Locate every blood parasite and identify its species.
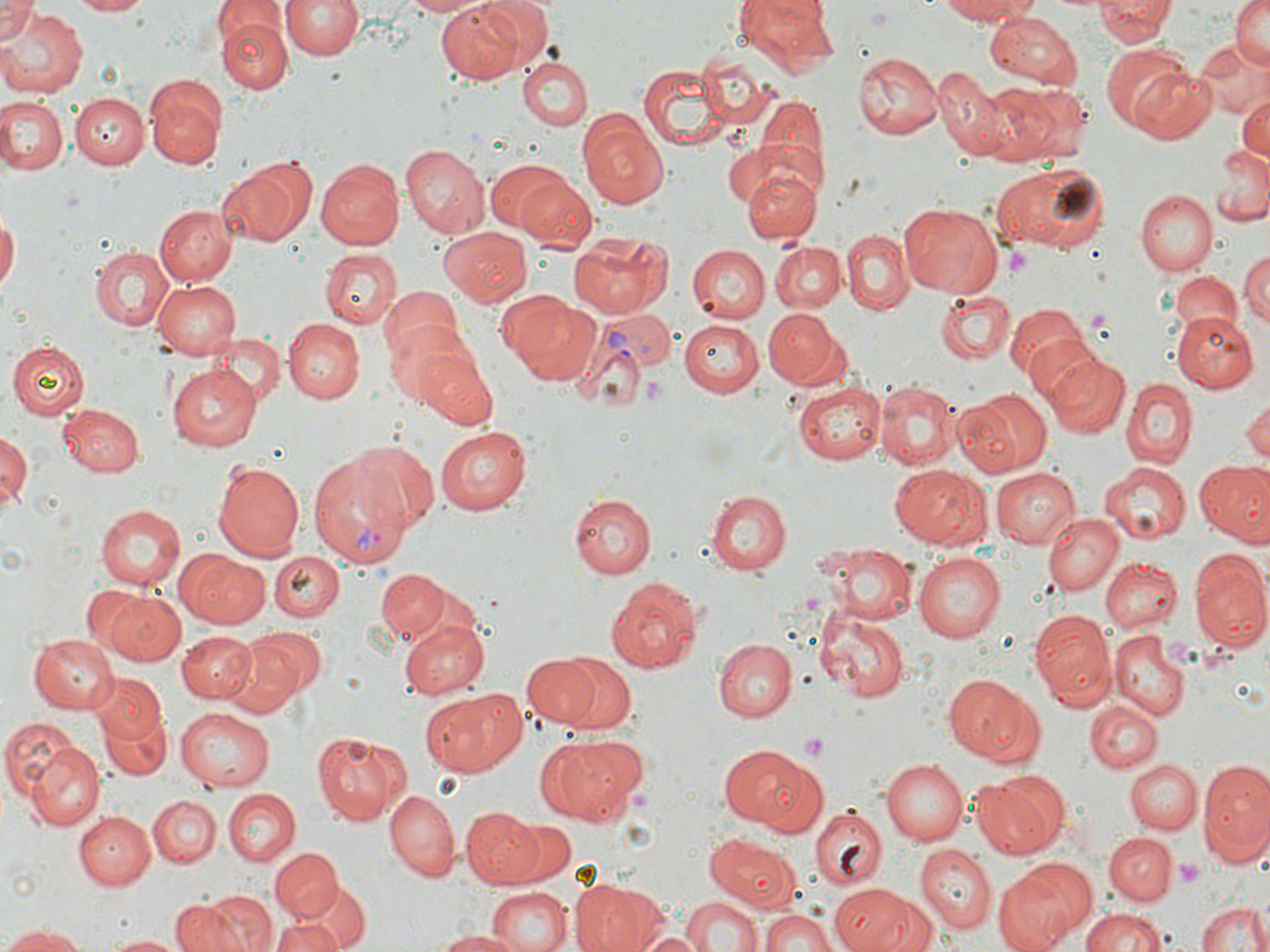

Approximate bounding boxes as (x1, y1, x2, y2) in pixels.
Plasmodium vivax-infected red blood cells: (602, 311, 674, 373), (307, 451, 413, 568).
No Plasmodium falciparum, Plasmodium ovale, Plasmodium malariae, Babesia divergens, or Trypanosoma brucei observed.

slide_level_diagnosis: Plasmodium vivax
platelet_locations: 'approximate bounding boxes as (x1, y1, x2, y2) in pixels: (1004, 245, 1034, 281), (643, 376, 666, 405), (799, 734, 830, 762), (1172, 859, 1205, 889)'
magnification: 1000x
modality: optical microscopy
field_of_view: one of a larger specimen
uninfected_red_blood_cell_locations: 'approximate bounding boxes as (x1, y1, x2, y2) in pixels: (73, 0, 149, 17), (281, 0, 364, 59), (402, 0, 493, 17), (472, 0, 555, 73), (731, 0, 838, 72), (934, 0, 1046, 25), (1230, 0, 1270, 68), (0, 1, 39, 44), (436, 1, 526, 84), (1095, 1, 1174, 48), (214, 3, 287, 48), (0, 8, 86, 96), (984, 11, 1086, 88), (221, 18, 291, 92), (1191, 37, 1269, 120), (1104, 44, 1195, 132), (699, 51, 767, 127), (853, 53, 942, 141), (517, 57, 591, 132), (638, 65, 729, 149), (1128, 66, 1217, 143), (933, 69, 1020, 161), (989, 80, 1084, 162), (146, 84, 224, 170), (0, 95, 66, 177), (71, 95, 147, 168), (749, 95, 827, 198), (1236, 98, 1270, 164), (579, 110, 670, 208), (728, 126, 823, 224), (402, 143, 489, 237), (1214, 144, 1269, 227), (314, 158, 402, 250), (487, 160, 575, 234), (217, 162, 304, 247), (992, 162, 1111, 252), (742, 166, 821, 244), (516, 176, 597, 250), (1138, 189, 1219, 274), (897, 203, 1003, 298), (154, 204, 238, 285), (0, 212, 19, 292), (439, 227, 532, 307), (841, 231, 914, 316), (570, 232, 667, 318), (770, 242, 843, 311), (89, 245, 173, 331), (686, 245, 769, 322), (1238, 248, 1270, 336), (320, 249, 400, 329), (1168, 273, 1242, 343), (153, 277, 241, 358), (378, 288, 462, 366), (505, 291, 604, 385), (934, 291, 1016, 363), (1006, 302, 1094, 384), (762, 306, 842, 386), (1172, 311, 1258, 392), (282, 317, 365, 402), (386, 320, 477, 409), (680, 320, 763, 397), (215, 333, 285, 407), (1025, 335, 1111, 412), (8, 341, 90, 419), (413, 348, 499, 428), (1044, 353, 1130, 437), (167, 363, 262, 450), (796, 378, 887, 464), (875, 378, 960, 469), (1122, 379, 1196, 466), (956, 387, 1051, 477), (1240, 394, 1270, 466), (59, 404, 144, 476), (436, 427, 531, 514), (1, 429, 33, 518), (352, 440, 437, 527), (213, 459, 306, 560), (1193, 460, 1270, 543), (1099, 462, 1188, 546), (889, 465, 993, 549), (991, 467, 1081, 549), (709, 489, 791, 576), (568, 492, 657, 580), (97, 504, 187, 590), (1043, 512, 1124, 596), (819, 543, 919, 624), (270, 549, 345, 620), (184, 552, 273, 629), (915, 552, 1005, 641), (1189, 552, 1270, 650), (1100, 557, 1179, 632), (375, 568, 452, 639), (605, 575, 704, 675), (103, 589, 185, 665), (816, 609, 909, 701), (1030, 612, 1114, 707), (402, 617, 491, 700), (239, 627, 325, 709), (177, 631, 255, 704), (28, 632, 118, 711), (1109, 632, 1188, 720), (713, 638, 795, 719), (224, 647, 300, 719), (548, 650, 640, 738), (522, 655, 606, 727), (91, 674, 166, 747), (945, 676, 1041, 765), (420, 688, 528, 776), (1085, 700, 1161, 772), (96, 703, 170, 780), (175, 709, 274, 790), (1, 719, 89, 822), (312, 731, 399, 822), (536, 735, 643, 825), (29, 739, 105, 830), (720, 742, 820, 829), (1198, 758, 1270, 864), (881, 759, 967, 845), (1125, 759, 1202, 835), (974, 770, 1067, 859), (223, 788, 301, 866), (384, 789, 459, 881), (148, 795, 221, 867), (377, 798, 539, 879), (809, 806, 887, 889), (462, 808, 543, 887), (76, 810, 155, 889), (506, 816, 577, 885), (1103, 832, 1177, 905), (706, 835, 803, 913), (915, 845, 997, 933), (271, 848, 344, 923), (993, 864, 1084, 952), (569, 879, 654, 952), (299, 880, 374, 947), (829, 884, 912, 951), (487, 888, 571, 952), (207, 890, 278, 952), (681, 895, 761, 952), (861, 895, 937, 952), (172, 896, 251, 952), (1195, 897, 1268, 952), (757, 906, 837, 952), (1079, 907, 1173, 952), (273, 913, 347, 952), (1, 925, 90, 951), (437, 930, 532, 952), (639, 931, 707, 952), (103, 932, 182, 951)'
preparation: thin blood smear
image_size: 1270×952 pixels
stain: May-Grünwald-Giemsa